Report the malaria status of this cell.
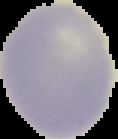
Uninfected.

Summary:
  - Image type: cell region segmented out of the field of view; surrounding area masked to black
  - Image size: 118×139 pixels
  - Preparation: thin blood smear